Describe the morphology of the red blood cells.
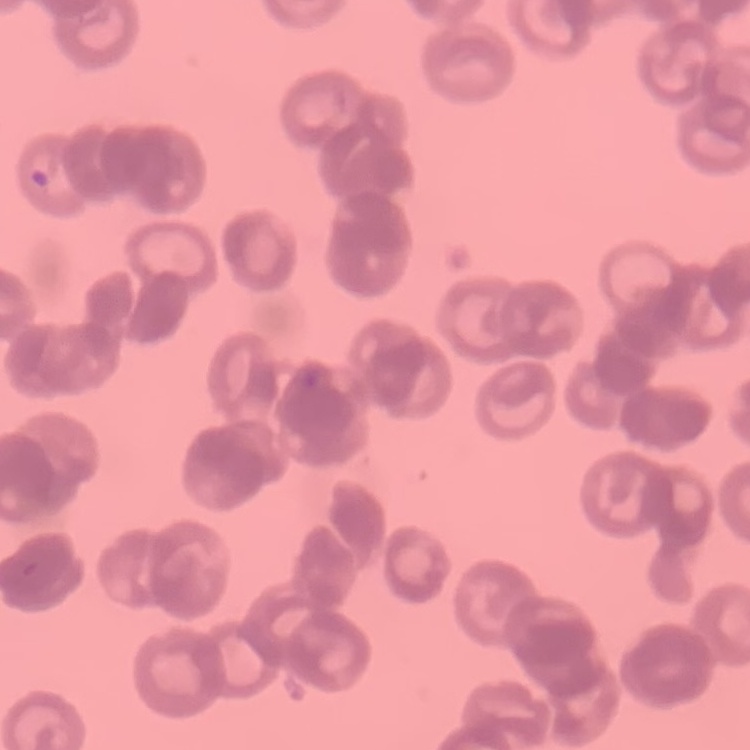

Rouleaux formation.

stain = Field's or Giemsa
image type = one tile cut from a larger photomicrograph
preparation = thin blood smear